Locate every blood parasite and identify its species.
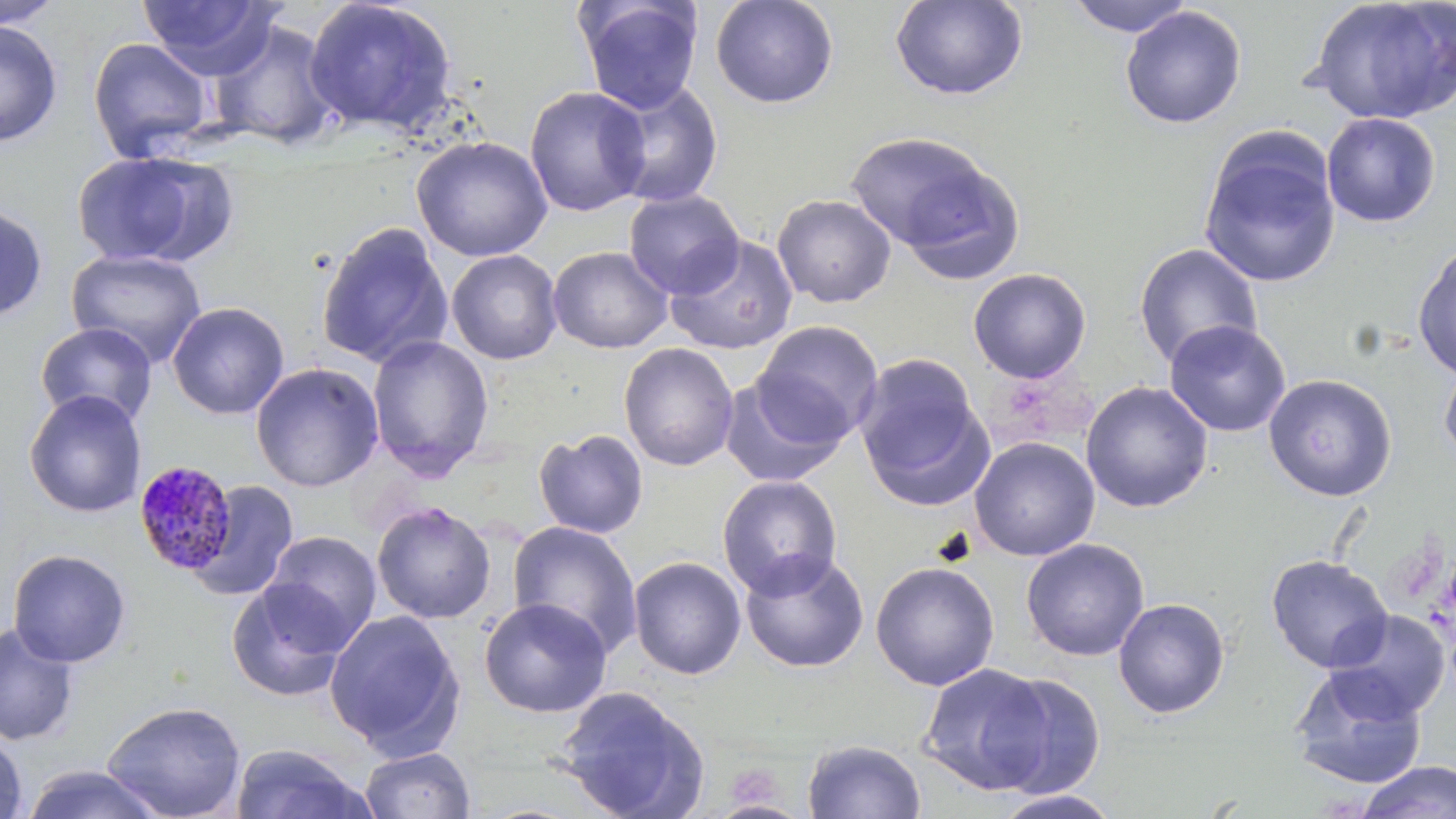
Approximate bounding boxes as named x1/y1/x2/y2 corners in pixels.
Plasmodium malariae-infected red blood cells: (x1=132, y1=458, x2=239, y2=577).
No Plasmodium falciparum, Plasmodium ovale, Plasmodium vivax, Babesia divergens, or Trypanosoma brucei observed.

slide-level diagnosis = Plasmodium malariae
magnification = 1000x
modality = light microscopy
uninfected red blood cell locations = approximate bounding boxes as named x1/y1/x2/y2 corners in pixels: (x1=0, y1=0, x2=64, y2=29), (x1=138, y1=0, x2=282, y2=79), (x1=303, y1=0, x2=459, y2=137), (x1=575, y1=0, x2=703, y2=114), (x1=709, y1=0, x2=840, y2=109), (x1=889, y1=0, x2=1029, y2=102), (x1=1065, y1=0, x2=1197, y2=38), (x1=1308, y1=0, x2=1456, y2=125), (x1=1120, y1=6, x2=1247, y2=129), (x1=209, y1=18, x2=342, y2=150), (x1=0, y1=20, x2=63, y2=147), (x1=87, y1=37, x2=214, y2=161), (x1=603, y1=79, x2=725, y2=208), (x1=524, y1=86, x2=651, y2=218), (x1=1321, y1=112, x2=1441, y2=227), (x1=1199, y1=129, x2=1342, y2=290), (x1=844, y1=130, x2=1004, y2=258), (x1=412, y1=136, x2=553, y2=262), (x1=71, y1=150, x2=228, y2=268), (x1=893, y1=160, x2=1026, y2=284), (x1=624, y1=190, x2=745, y2=299), (x1=772, y1=194, x2=896, y2=308), (x1=0, y1=203, x2=49, y2=322), (x1=315, y1=221, x2=453, y2=369), (x1=664, y1=235, x2=798, y2=356), (x1=1133, y1=242, x2=1263, y2=369), (x1=548, y1=246, x2=673, y2=353), (x1=1412, y1=246, x2=1456, y2=381), (x1=66, y1=249, x2=207, y2=367), (x1=446, y1=249, x2=563, y2=364), (x1=968, y1=267, x2=1092, y2=384), (x1=167, y1=301, x2=290, y2=420), (x1=1164, y1=320, x2=1291, y2=437), (x1=753, y1=321, x2=884, y2=443), (x1=34, y1=322, x2=158, y2=428), (x1=367, y1=335, x2=495, y2=480), (x1=618, y1=342, x2=740, y2=472), (x1=853, y1=354, x2=991, y2=508), (x1=1439, y1=357, x2=1456, y2=467), (x1=251, y1=362, x2=385, y2=492), (x1=1263, y1=373, x2=1397, y2=501), (x1=720, y1=375, x2=848, y2=488), (x1=1080, y1=381, x2=1214, y2=513), (x1=23, y1=389, x2=147, y2=518), (x1=533, y1=429, x2=649, y2=539), (x1=969, y1=436, x2=1100, y2=561), (x1=717, y1=474, x2=842, y2=598), (x1=188, y1=480, x2=300, y2=601), (x1=371, y1=502, x2=495, y2=624), (x1=506, y1=520, x2=643, y2=659), (x1=262, y1=531, x2=382, y2=648), (x1=1020, y1=538, x2=1150, y2=662), (x1=7, y1=549, x2=132, y2=667), (x1=739, y1=550, x2=869, y2=673), (x1=1266, y1=554, x2=1393, y2=673), (x1=628, y1=556, x2=747, y2=679), (x1=870, y1=561, x2=1000, y2=691), (x1=226, y1=580, x2=352, y2=702), (x1=478, y1=598, x2=612, y2=718), (x1=1113, y1=598, x2=1230, y2=719), (x1=324, y1=609, x2=465, y2=757), (x1=1326, y1=609, x2=1451, y2=722), (x1=0, y1=624, x2=79, y2=747), (x1=919, y1=663, x2=1056, y2=795), (x1=1290, y1=665, x2=1427, y2=790), (x1=986, y1=672, x2=1107, y2=798), (x1=556, y1=686, x2=710, y2=819), (x1=101, y1=700, x2=247, y2=819), (x1=0, y1=726, x2=28, y2=819), (x1=802, y1=739, x2=926, y2=819), (x1=229, y1=742, x2=371, y2=819), (x1=360, y1=747, x2=475, y2=819), (x1=1356, y1=761, x2=1456, y2=819), (x1=20, y1=764, x2=167, y2=819), (x1=995, y1=790, x2=1121, y2=819)
stain = May-Grünwald-Giemsa
field of view = single
preparation = thin blood smear
image size = 1456×819 pixels